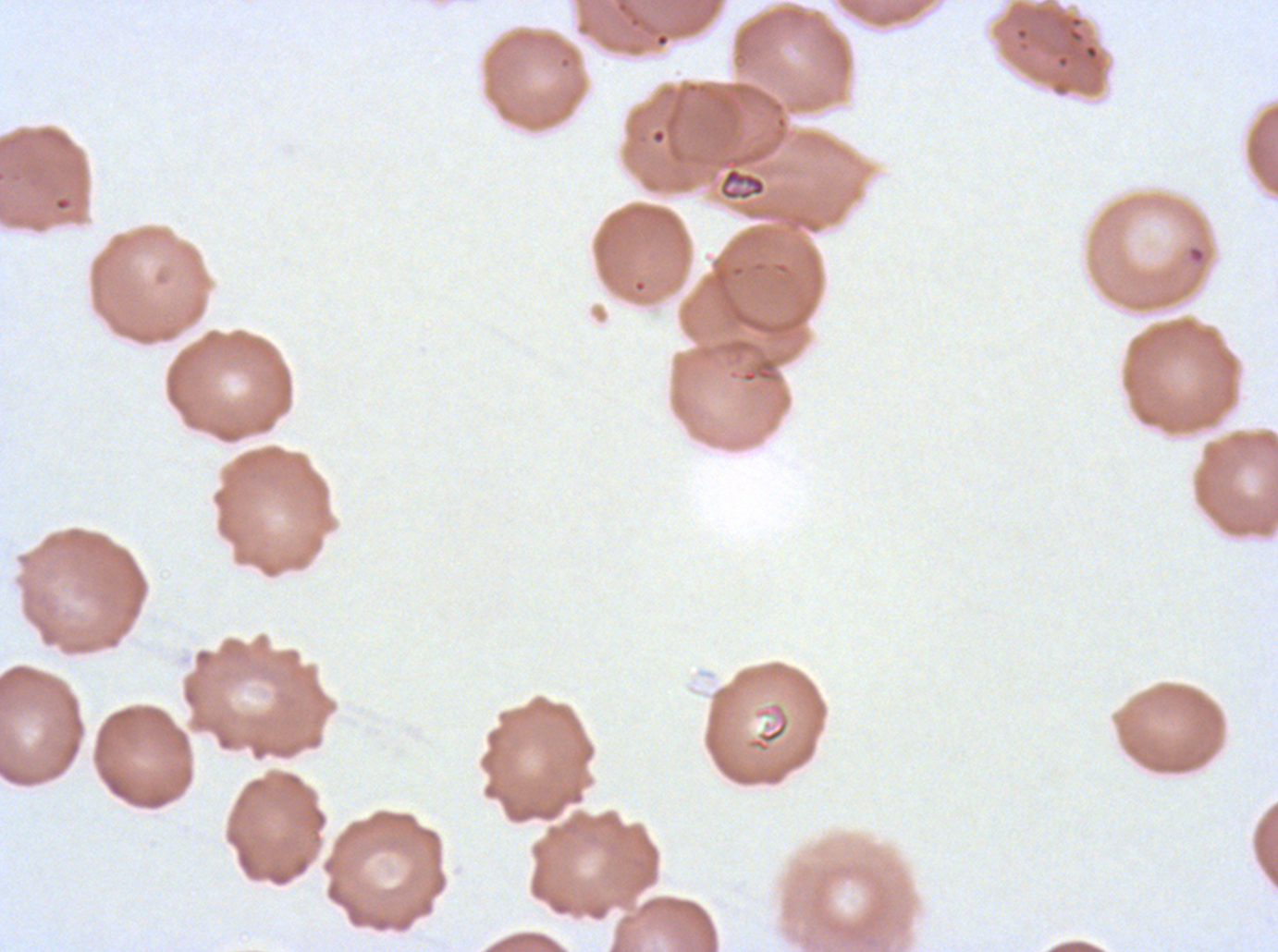

Approximate bounding boxes as {x1, y1, x2, y2} in pixels.
Summary:
  - Debris locations: {719, 166, 767, 201}
  - Stain: Giemsa
  - Image size: 1278×952 pixels
  - Specimen: Plasmodium falciparum cultured ex vivo for 24 to 48 hours, from a patient in The Gambia
  - Field of view: one sub-image of a larger composite
  - Preparation: thin blood film